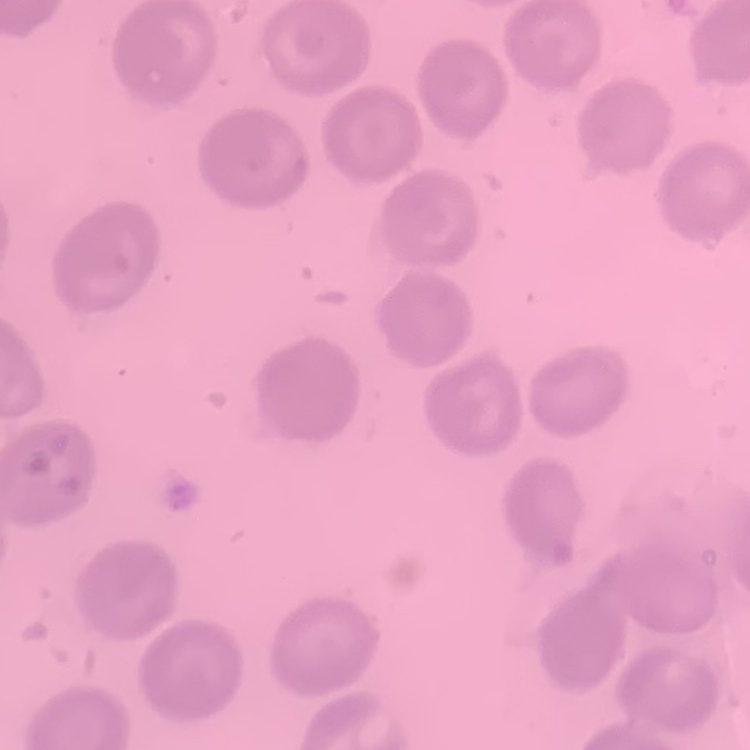

Summary:
  - Erythrocyte morphology: no rouleaux formation
  - Preparation: thin peripheral smear
  - Image type: square crop of a larger photomicrograph
  - Stain: Field's or Giemsa